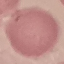

malaria status = uninfected
stain = Giemsa
preparation = thin smear
image type = automatically extracted cell patch, resized to 64 × 64 pixels
capture = smartphone through the microscope eyepiece